Outline each blood parasite and name the species.
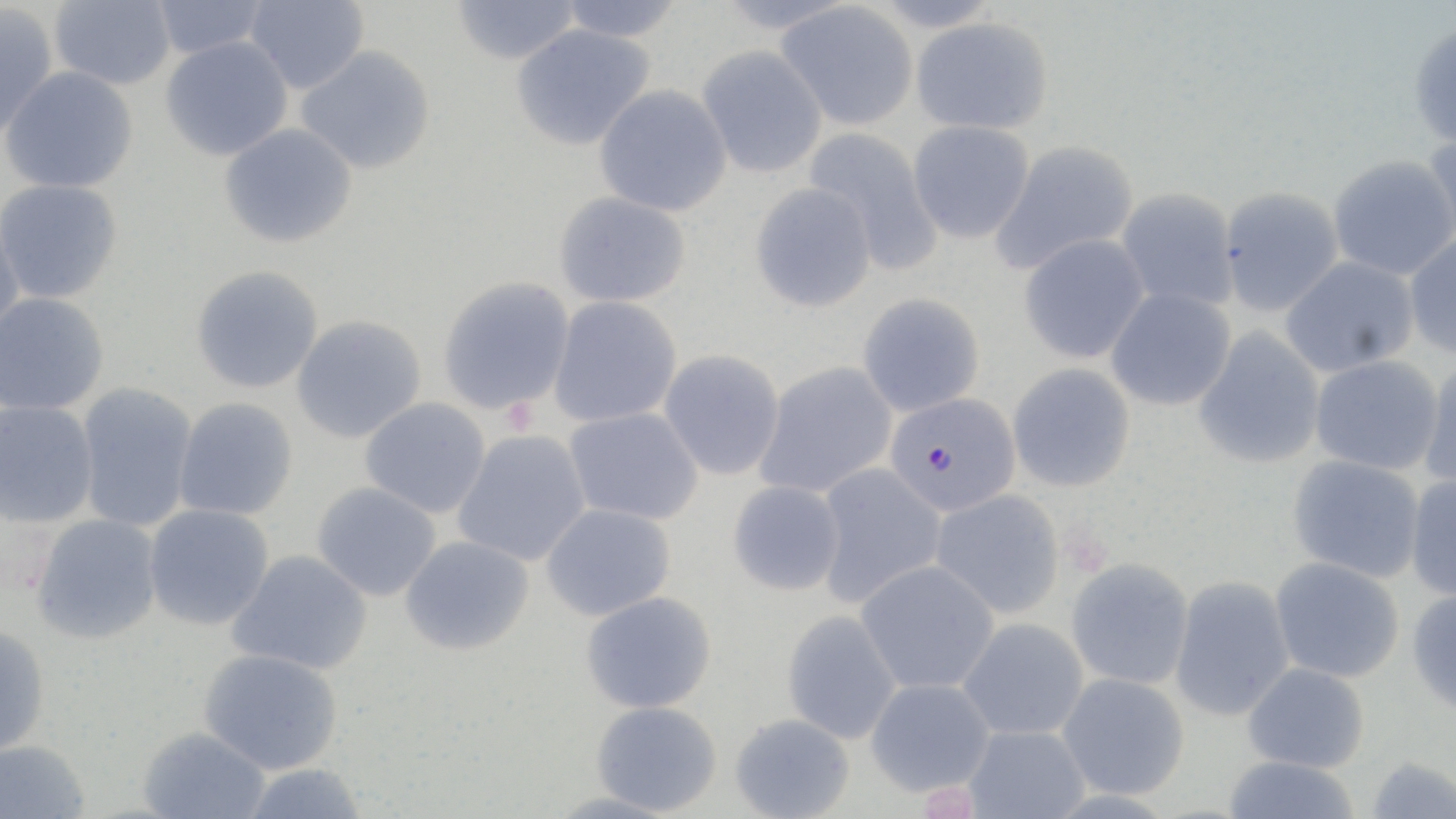
Approximate bounding boxes as (x1, y1, x2, y2) in pixels.
Plasmodium falciparum-infected red blood cells: (884, 392, 1020, 516).
No Plasmodium ovale, Plasmodium malariae, Plasmodium vivax, Babesia divergens, or Trypanosoma brucei observed.

Uninfected red blood cell locations: (149, 0, 269, 60), (244, 0, 370, 95), (450, 0, 581, 65), (49, 1, 176, 90), (555, 1, 686, 42), (776, 2, 918, 130), (0, 3, 59, 140), (911, 17, 1053, 135), (1408, 21, 1456, 149), (511, 23, 655, 151), (160, 36, 293, 161), (296, 45, 436, 174), (696, 45, 828, 179), (1, 66, 138, 194), (594, 84, 732, 217), (907, 120, 1035, 244), (219, 123, 357, 248), (803, 127, 943, 274), (1423, 131, 1456, 248), (991, 139, 1140, 275), (1327, 155, 1456, 281), (0, 178, 123, 304), (750, 182, 877, 312), (1116, 187, 1239, 312), (1218, 187, 1343, 316), (554, 191, 691, 308), (0, 213, 24, 346), (1018, 233, 1150, 364), (1404, 234, 1456, 360), (1280, 256, 1419, 377), (190, 265, 324, 394), (437, 277, 575, 415), (1105, 287, 1236, 411), (0, 292, 110, 416), (857, 292, 985, 417), (549, 296, 682, 427), (291, 314, 427, 444), (1194, 327, 1326, 469), (659, 349, 785, 481), (1310, 355, 1445, 475), (1419, 358, 1456, 492), (756, 361, 897, 499), (1007, 363, 1135, 492), (76, 382, 198, 532), (173, 397, 299, 521), (359, 397, 491, 518), (0, 400, 98, 528), (564, 407, 703, 525), (452, 429, 591, 567), (1287, 455, 1425, 583), (814, 463, 946, 607), (1405, 474, 1456, 602), (727, 480, 844, 596), (311, 482, 441, 602), (930, 489, 1065, 619), (540, 503, 677, 620), (143, 504, 275, 631), (31, 514, 163, 645), (399, 535, 535, 656), (227, 550, 373, 676), (1065, 557, 1194, 690), (1270, 557, 1404, 683), (855, 560, 999, 695), (1169, 575, 1295, 722), (1407, 588, 1456, 716), (580, 591, 718, 714), (781, 610, 902, 744), (957, 617, 1089, 741), (0, 624, 51, 758), (198, 648, 344, 774), (1242, 662, 1370, 773), (1057, 672, 1190, 800), (865, 678, 995, 796), (589, 701, 722, 816), (729, 713, 855, 819), (963, 724, 1090, 818), (138, 726, 271, 818), (0, 739, 91, 819), (1221, 755, 1362, 819), (1364, 756, 1456, 818), (238, 762, 369, 819), (544, 791, 682, 819). Slide-level diagnosis: Plasmodium falciparum. Thin blood film. Light microscopy. Image is 1456×819 pixels. One field of a larger specimen. May-Grünwald-Giemsa stain. 1000x magnification.